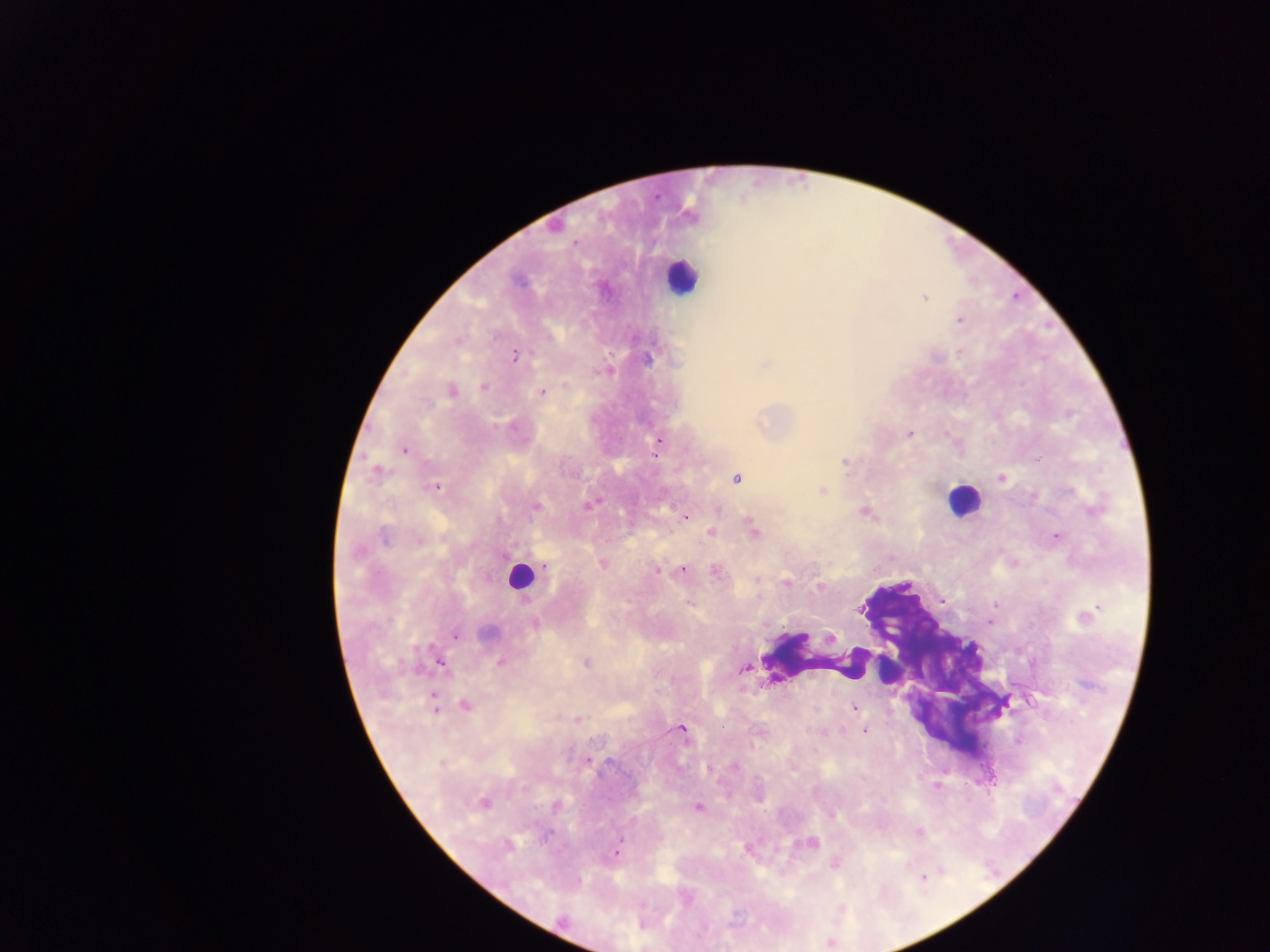

Approximate centers as {x, y} in pixels.
Summary:
  - Leukocyte locations: {681, 276}, {962, 500}, {520, 576}, {889, 669}
  - Malaria parasite locations: {924, 297}, {960, 319}, {458, 340}, {515, 356}, {646, 359}, {765, 365}, {599, 372}, {566, 385}, {484, 387}, {452, 391}, {542, 392}, {910, 434}, {658, 444}, {404, 450}, {844, 462}, {377, 471}, {736, 478}, {1002, 479}, {434, 486}, {822, 491}, {588, 506}, {535, 507}, {864, 512}, {685, 516}, {753, 531}, {712, 533}, {384, 536}, {1056, 537}, {418, 541}, {358, 552}, {604, 563}, {658, 570}, {683, 570}, {716, 573}, {756, 579}, {786, 582}, {819, 587}, {995, 605}, {860, 609}, {1085, 616}, {535, 624}, {488, 632}, {455, 636}, {830, 637}, {500, 663}, {587, 663}, {442, 664}, {745, 669}, {434, 704}, {465, 705}, {854, 707}, {578, 720}, {722, 726}, {681, 729}, {864, 731}, {441, 763}, {734, 767}, {709, 769}, {483, 802}, {556, 806}, {698, 808}, {918, 833}, {811, 843}, {507, 845}, {617, 851}, {835, 864}, {923, 878}, {578, 881}, {564, 921}
  - Field of view: single
  - Image size: 1270×952 pixels
  - Preparation: thick blood film
  - Capture: mobile-phone photograph through a microscope
  - Country: Ghana